Report the malaria status of this cell.
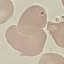
It is uninfected.

Summary:
  - Capture: smartphone camera at the microscope eyepiece
  - Image type: automatically extracted cell patch, resized to 64 × 64 pixels
  - Stain: Giemsa
  - Preparation: thin blood film